Identify the parasite.
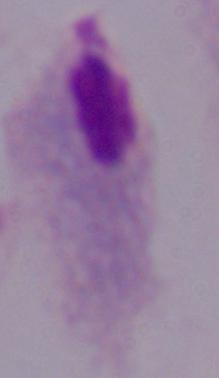
This is a trichomonad.

Summary:
  - Modality: photomicrograph
  - Magnification: 1000x